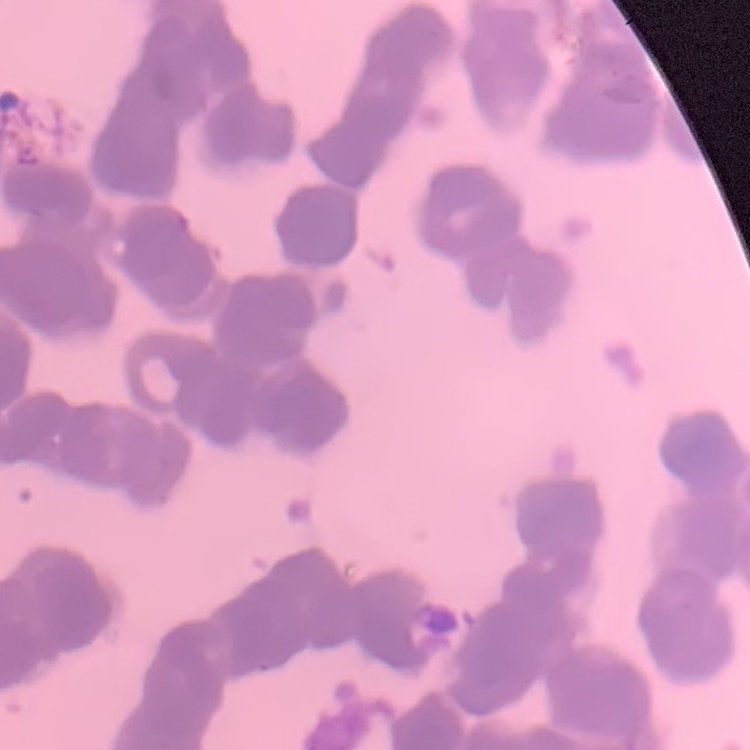
Summary:
  - Red blood cell morphology: rouleaux formation
  - Stain: Field's or Giemsa
  - Preparation: thin peripheral smear
  - Image type: square crop of a larger photomicrograph